Assess the morphology of the erythrocytes.
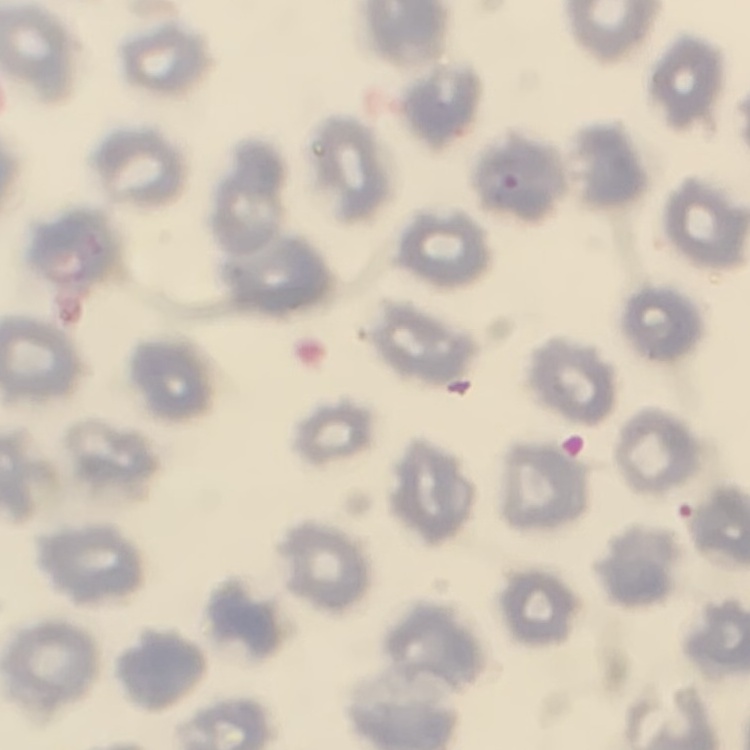

They show no rouleaux formation.

Summary:
  - Preparation: thin peripheral smear
  - Image type: square crop of a larger photomicrograph
  - Stain: Field's or Giemsa